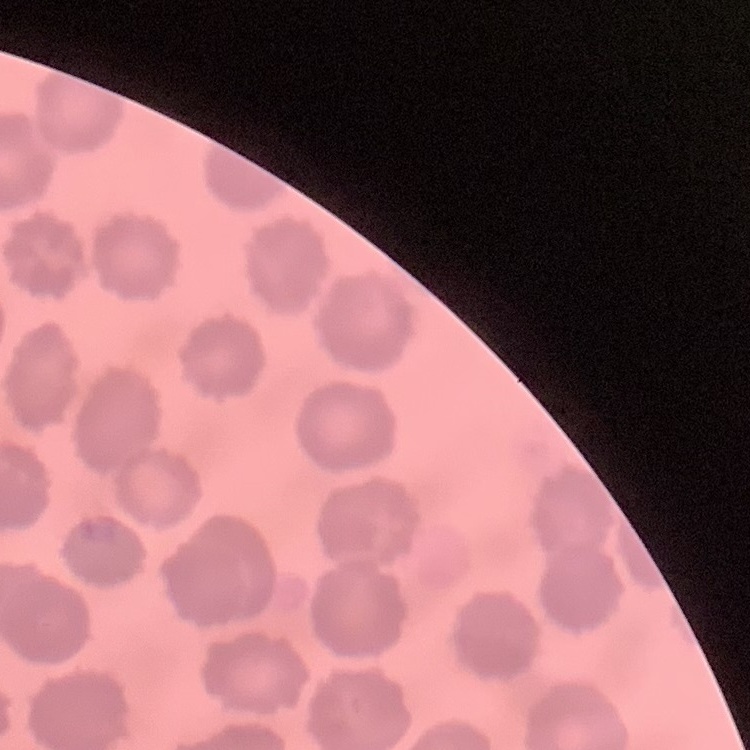

erythrocyte morphology = no rouleaux formation
preparation = thin blood smear
stain = Field's or Giemsa
image type = square crop of a larger photomicrograph